Report the malaria status of this cell.
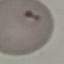

It is parasitized.

Summary:
  - Preparation: thin blood smear
  - Stain: Giemsa
  - Capture: smartphone camera at the microscope eyepiece
  - Image type: cell patch, automatically extracted from a larger field of view and resized to 64 × 64 pixels